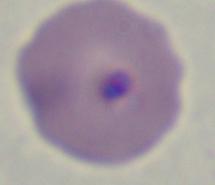
magnification = 1000x
modality = photomicrograph
identification = Babesia